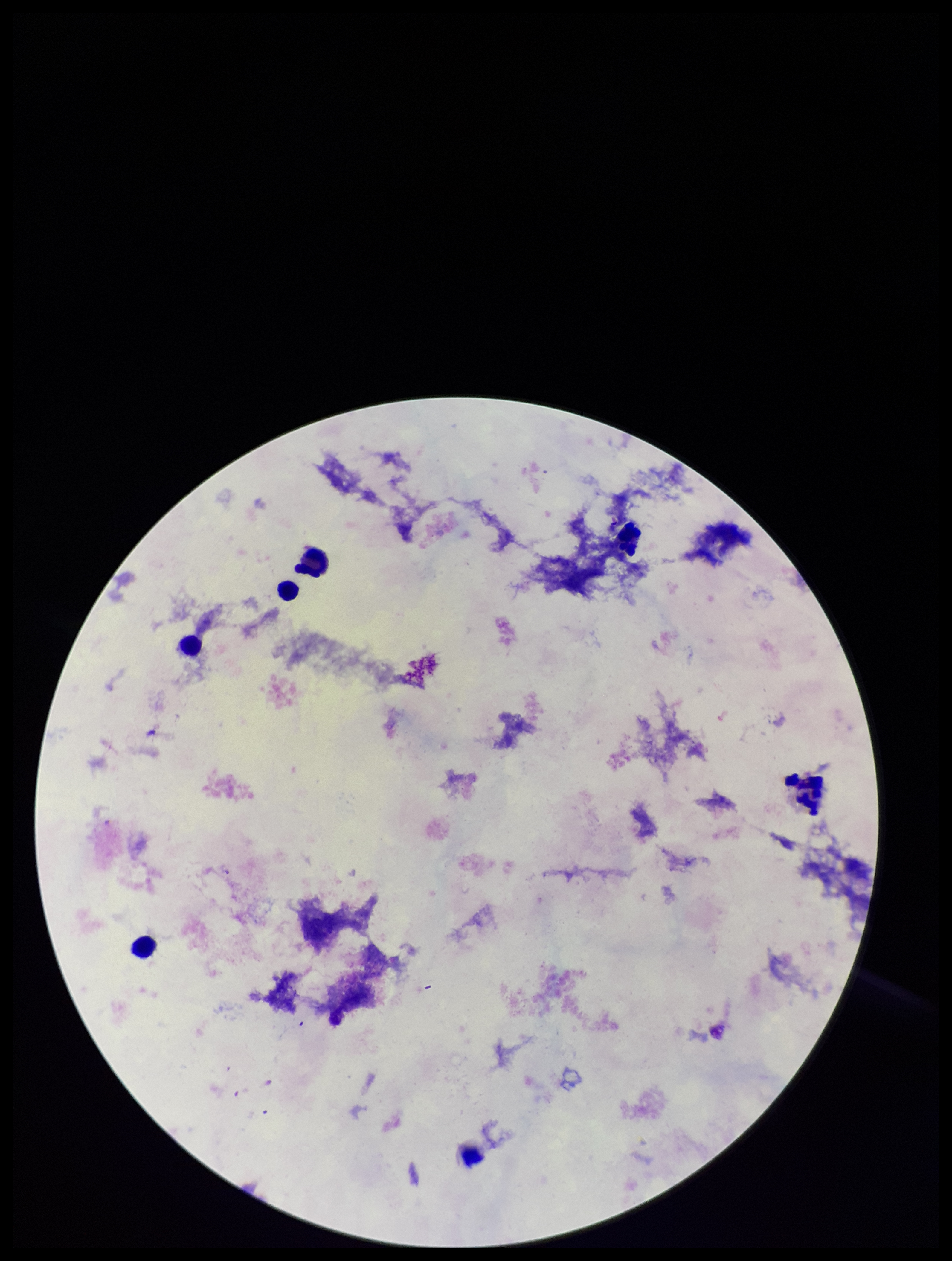

Summary:
  - Field of view: single
  - Plasmodium parasites: none identified
  - Patient malaria status: negative
  - Capture: smartphone photograph through the microscope eyepiece
  - Parasite count: 0
  - Preparation: thick blood smear
  - Stain: Giemsa
  - Leukocyte count: 6
  - Image size: 952×1261 pixels